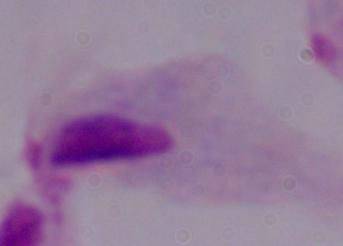
A trichomonad is shown. Captured at 1000x magnification. Photomicrograph.